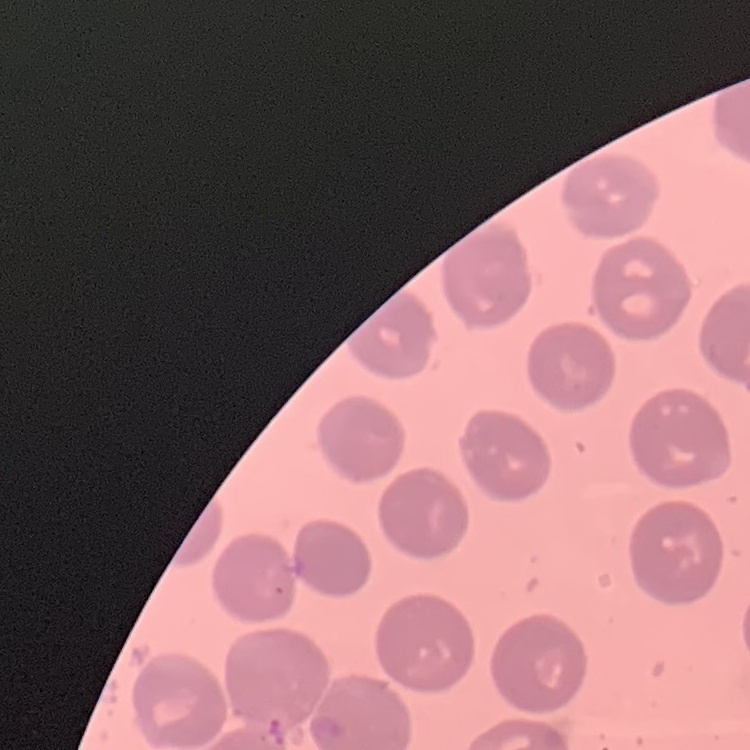
{
  "red_blood_cell_morphology": "no rouleaux formation",
  "image_type": "one tile cut from a larger photomicrograph",
  "stain": "Field's or Giemsa",
  "preparation": "thin blood film"
}